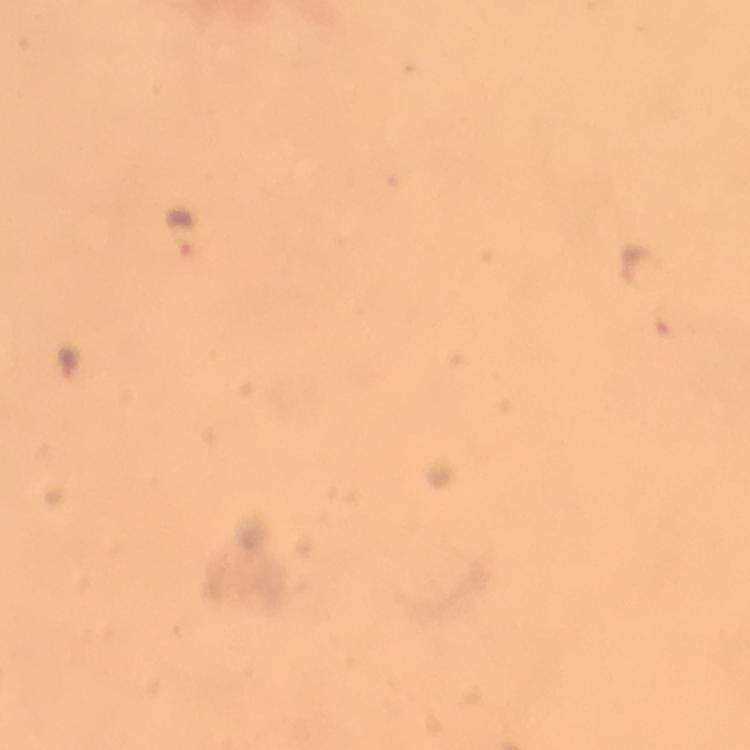

Approximate centers as [x, y] in pixels.
Summary:
  - Malaria parasite locations: [178, 232]
  - Context: from a diagnostic examination for malaria
  - Stain: Giemsa
  - Preparation: thick blood film
  - Cropped from: a single field of view
  - Immersion oil: applied
  - Image size: 750×750 pixels
  - Magnification: 100x
  - Capture: smartphone camera through the microscope